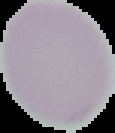
image type = segmented cell region with the area outside set to black
preparation = thin blood smear
image size = 115×133 pixels
malaria status = uninfected